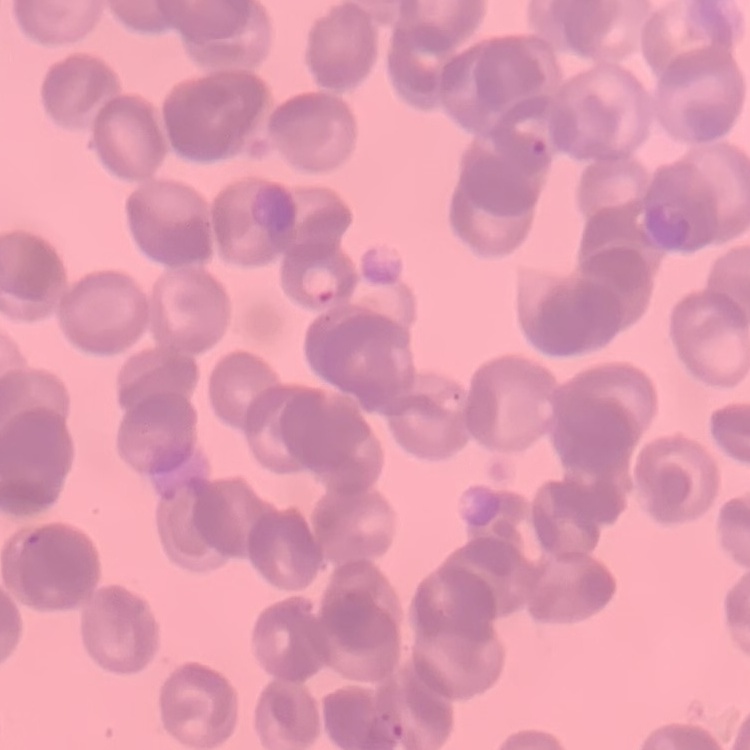

The erythrocytes exhibit rouleaux formation. One tile cut from a larger photomicrograph. Stained with either Field's or Giemsa. Thin peripheral smear.